Point out every Plasmodium parasite.
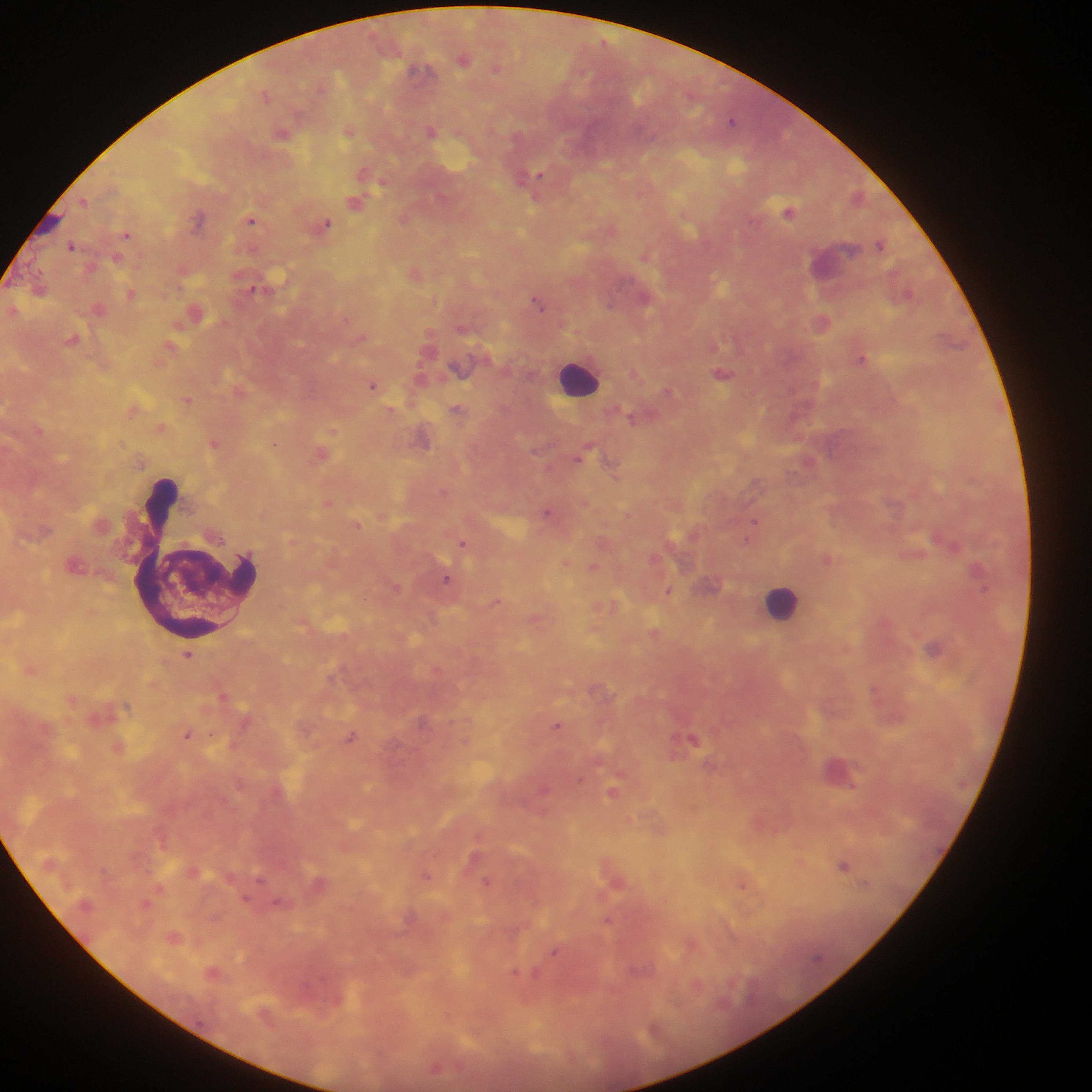

Approximate centers as [x, y] in pixels.
Plasmodium parasites: [464, 60], [496, 68], [417, 70], [265, 94], [731, 121], [431, 131], [348, 132], [282, 133], [538, 175], [381, 183], [84, 201], [355, 203], [789, 212], [198, 219], [403, 219], [251, 220], [326, 224], [127, 234], [879, 244], [71, 245], [646, 255], [253, 288], [130, 294], [537, 302], [609, 305], [823, 322], [361, 337], [862, 358], [723, 374], [373, 385], [668, 391], [188, 400], [456, 408], [631, 418], [333, 431], [213, 443], [274, 444], [584, 454], [546, 512], [755, 522], [357, 526], [938, 538], [463, 542], [593, 568], [977, 571], [447, 579], [668, 592], [496, 601], [933, 647], [188, 655], [557, 725], [187, 734], [351, 737], [692, 739], [613, 792], [844, 865], [427, 876], [260, 879], [485, 882], [743, 886], [608, 920], [554, 953].

preparation = thick blood film
country = Ghana
capture = mobile-phone photograph through a microscope
field of view = single
image size = 1092×1092 pixels
leukocyte locations = approximate centers as [x, y] in pixels: [578, 378], [195, 560], [781, 603]